Report the malaria status of this cell.
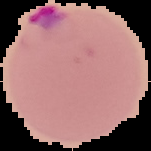

Parasitized.

Summary:
  - Preparation: thin blood film
  - Image size: 151×151 pixels
  - Image type: segmented cell region on a black background